Assess this cell for malaria.
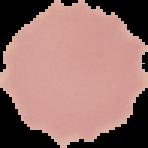
It is uninfected.

preparation = thin blood smear
image size = 148×148 pixels
image type = cell region segmented out of the field of view; surrounding area masked to black